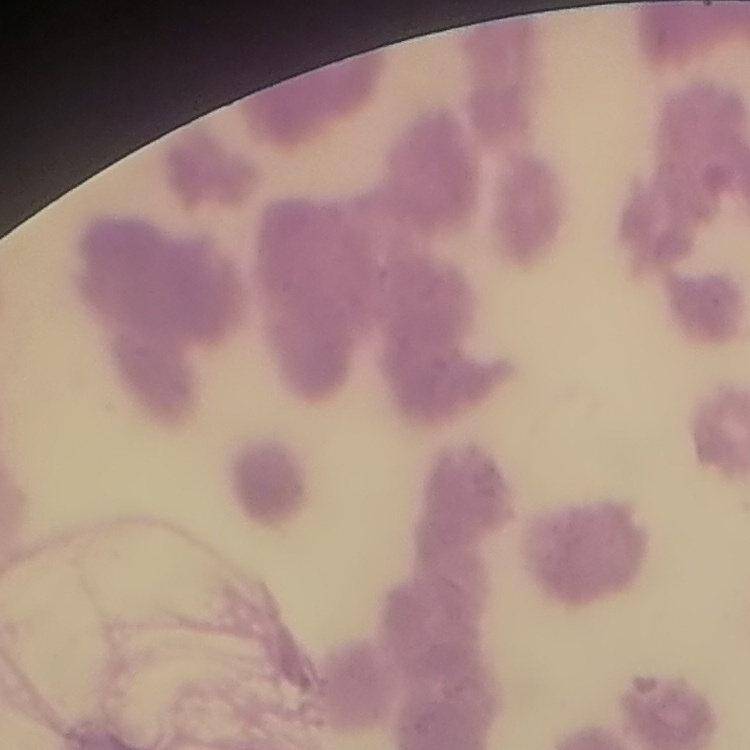

Summary:
  - Erythrocyte morphology: rouleaux formation
  - Preparation: thin peripheral smear
  - Stain: Field's or Giemsa
  - Image type: square crop of a larger photomicrograph